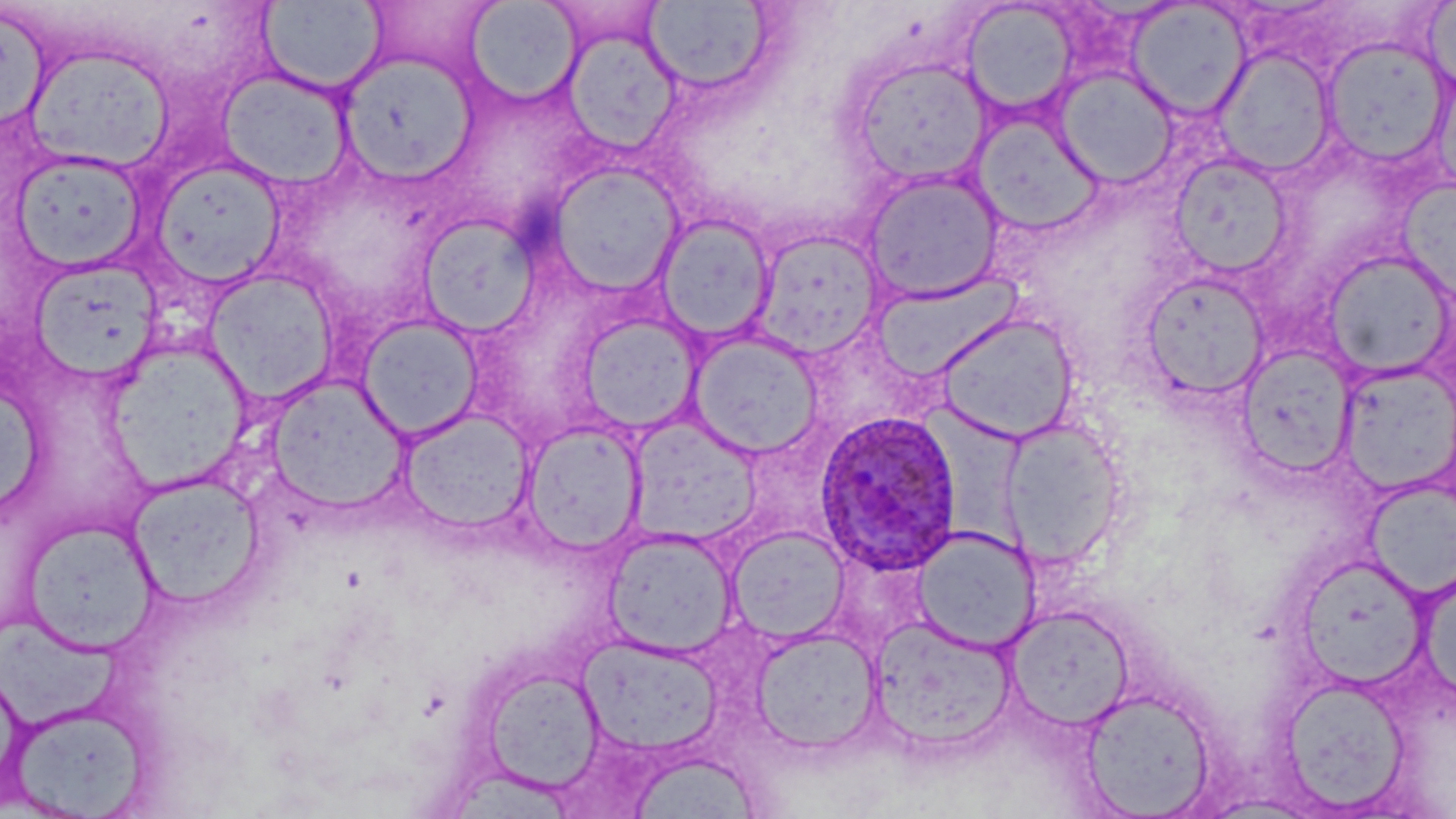

{
  "slide_level_diagnosis": "Plasmodium ovale",
  "modality": "optical microscopy",
  "stain": "May-Grünwald-Giemsa",
  "preparation": "thin blood smear",
  "magnification": "1000x",
  "uninfected_red_blood_cell_locations": "approximate bounding boxes as named x1/y1/x2/y2 corners in pixels: (x1=1421, y1=0, x2=1456, y2=103), (x1=258, y1=1, x2=385, y2=94), (x1=361, y1=1, x2=501, y2=80), (x1=464, y1=1, x2=581, y2=104), (x1=645, y1=1, x2=775, y2=94), (x1=961, y1=1, x2=1079, y2=116), (x1=1126, y1=3, x2=1250, y2=119), (x1=564, y1=28, x2=683, y2=155), (x1=1320, y1=38, x2=1451, y2=167), (x1=27, y1=47, x2=176, y2=172), (x1=1215, y1=47, x2=1336, y2=178), (x1=338, y1=54, x2=478, y2=183), (x1=849, y1=57, x2=991, y2=187), (x1=1052, y1=66, x2=1179, y2=190), (x1=218, y1=69, x2=353, y2=188), (x1=970, y1=110, x2=1105, y2=237), (x1=10, y1=149, x2=150, y2=272), (x1=1168, y1=153, x2=1294, y2=278), (x1=149, y1=157, x2=287, y2=289), (x1=547, y1=163, x2=684, y2=298), (x1=860, y1=170, x2=1005, y2=305), (x1=1398, y1=180, x2=1456, y2=304), (x1=418, y1=213, x2=541, y2=338), (x1=656, y1=213, x2=775, y2=344), (x1=749, y1=229, x2=886, y2=360), (x1=1321, y1=250, x2=1454, y2=381), (x1=29, y1=258, x2=163, y2=383), (x1=203, y1=268, x2=339, y2=407), (x1=1140, y1=271, x2=1271, y2=402), (x1=871, y1=272, x2=1024, y2=381), (x1=577, y1=311, x2=704, y2=434), (x1=933, y1=311, x2=1081, y2=444), (x1=357, y1=315, x2=485, y2=442), (x1=688, y1=330, x2=824, y2=458), (x1=104, y1=340, x2=254, y2=492), (x1=1236, y1=344, x2=1357, y2=477), (x1=1337, y1=362, x2=1455, y2=497), (x1=265, y1=374, x2=410, y2=514), (x1=0, y1=377, x2=45, y2=523), (x1=397, y1=409, x2=535, y2=535), (x1=628, y1=415, x2=763, y2=542), (x1=997, y1=417, x2=1128, y2=569), (x1=520, y1=422, x2=647, y2=554), (x1=127, y1=472, x2=265, y2=610), (x1=1364, y1=480, x2=1456, y2=601), (x1=21, y1=517, x2=160, y2=653), (x1=728, y1=525, x2=850, y2=643), (x1=912, y1=527, x2=1041, y2=653), (x1=602, y1=529, x2=737, y2=657), (x1=1003, y1=604, x2=1136, y2=732), (x1=869, y1=616, x2=1016, y2=754), (x1=751, y1=627, x2=883, y2=754), (x1=579, y1=636, x2=724, y2=757), (x1=479, y1=665, x2=608, y2=794), (x1=1278, y1=675, x2=1413, y2=814), (x1=1078, y1=689, x2=1216, y2=817), (x1=7, y1=700, x2=156, y2=818)",
  "image_size": "1456×819 pixels",
  "plasmodium_ovale_infected_red_blood_cell_locations": "approximate bounding boxes as named x1/y1/x2/y2 corners in pixels: (x1=813, y1=409, x2=965, y2=575)",
  "field_of_view": "one of a larger specimen"
}